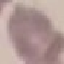

Malaria status: uninfected. Giemsa stain. Automatically extracted cell patch, resized to 64 × 64 pixels. Photographed with a smartphone camera at the microscope eyepiece. Thin blood smear.